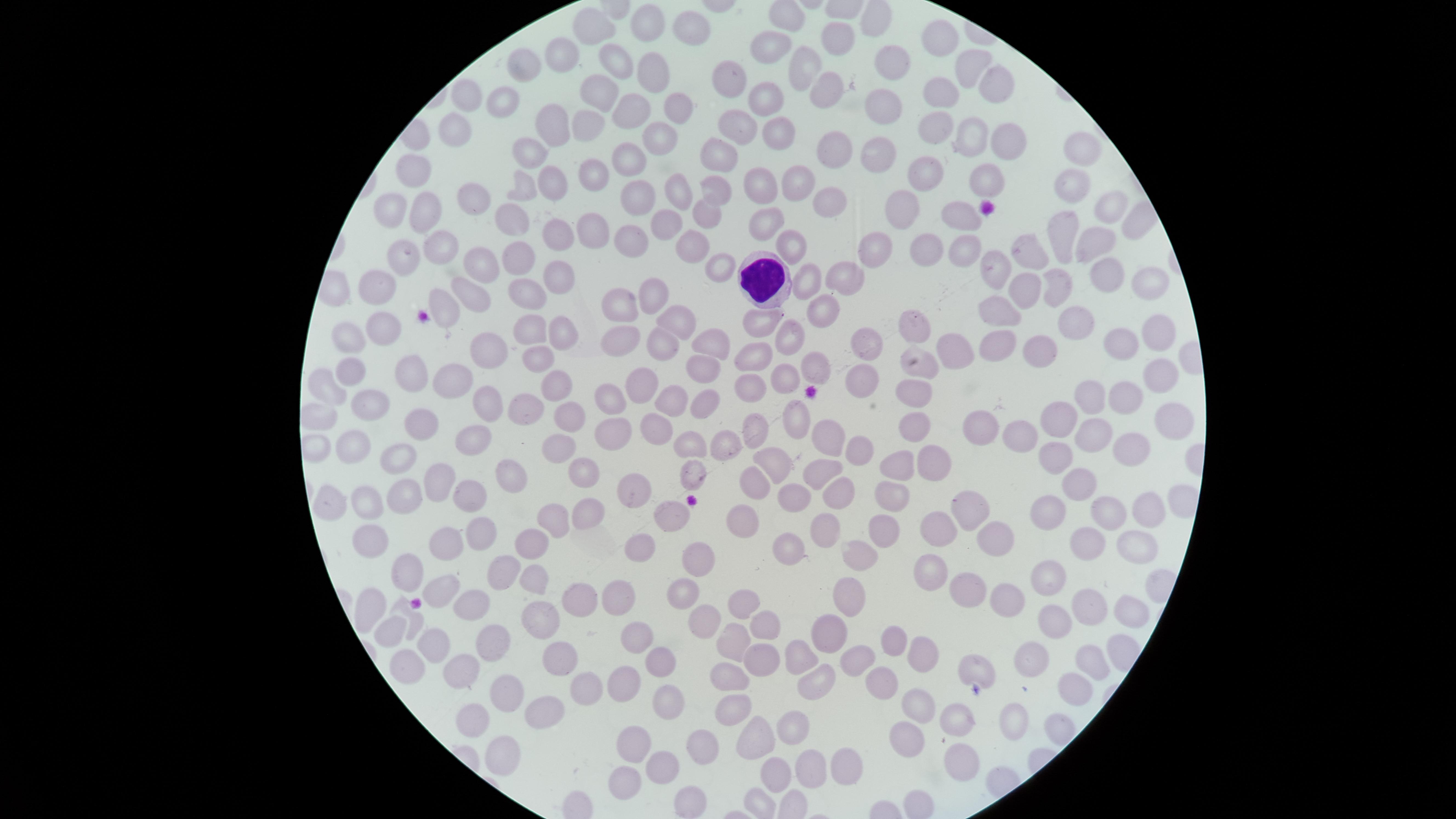
Approximate marker points as {x, y} in pixels. WBCs: {766, 276}. Uninfected RBCs: {782, 17}, {875, 23}, {649, 24}, {600, 27}, {690, 27}, {945, 37}, {839, 39}, {766, 46}, {530, 60}, {562, 61}, {889, 61}, {620, 62}, {808, 67}, {973, 68}, {655, 75}, {997, 81}, {726, 84}, {827, 87}, {943, 87}, {508, 93}, {469, 94}, {599, 95}, {885, 100}, {765, 102}, {672, 110}, {631, 114}, {455, 125}, {553, 125}, {735, 125}, {587, 126}, {774, 127}, {939, 131}, {998, 135}, {656, 136}, {968, 138}, {534, 148}, {717, 149}, {877, 149}, {829, 151}, {1079, 154}, {626, 163}, {419, 170}, {589, 173}, {552, 180}, {926, 180}, {983, 180}, {793, 182}, {764, 183}, {520, 184}, {1071, 188}, {679, 189}, {716, 189}, {473, 194}, {630, 194}, {830, 195}, {387, 202}, {1105, 207}, {960, 208}, {907, 209}, {417, 214}, {519, 214}, {708, 216}, {665, 222}, {769, 225}, {583, 231}, {553, 233}, {627, 234}, {1062, 238}, {1097, 242}, {791, 244}, {442, 246}, {696, 247}, {933, 249}, {395, 250}, {877, 250}, {518, 251}, {966, 251}, {1034, 254}, {992, 263}, {478, 264}, {719, 270}, {847, 272}, {1108, 273}, {561, 276}, {1149, 279}, {809, 280}, {380, 282}, {1028, 287}, {526, 288}, {1060, 288}, {653, 290}, {474, 298}, {623, 304}, {444, 308}, {827, 309}, {1001, 312}, {678, 318}, {379, 319}, {765, 320}, {1071, 325}, {920, 326}, {529, 327}, {561, 329}, {1150, 330}, {796, 335}, {621, 336}, {353, 342}, {704, 344}, {864, 344}, {660, 345}, {1114, 345}, {485, 347}, {1039, 348}, {956, 350}, {997, 351}, {756, 353}, {538, 355}, {923, 362}, {813, 365}, {351, 370}, {704, 372}, {405, 376}, {1156, 376}, {783, 378}, {557, 381}, {860, 381}, {448, 384}, {327, 386}, {644, 386}, {749, 387}, {918, 387}, {614, 394}, {1123, 395}, {1082, 398}, {670, 399}, {708, 401}, {488, 402}, {367, 403}, {530, 409}, {793, 415}, {322, 416}, {420, 417}, {569, 417}, {1053, 419}, {1177, 420}, {911, 421}, {980, 425}, {615, 429}, {751, 429}, {659, 433}, {821, 433}, {1091, 433}, {1016, 434}, {473, 438}, {722, 443}, {350, 444}, {692, 444}, {317, 445}, {555, 446}, {1132, 446}, {863, 454}, {1064, 454}, {389, 457}, {935, 457}, {781, 463}, {897, 464}, {827, 471}, {582, 472}, {509, 476}, {1085, 482}, {439, 483}, {758, 488}, {838, 490}, {891, 490}, {630, 492}, {470, 493}, {795, 494}, {394, 496}, {362, 503}, {1054, 503}, {330, 505}, {972, 505}, {1144, 510}, {673, 513}, {1118, 513}, {584, 515}, {551, 517}, {747, 521}, {827, 527}, {883, 528}, {940, 528}, {1089, 530}, {476, 532}, {439, 537}, {995, 537}, {368, 543}, {534, 546}, {636, 547}, {787, 549}, {1127, 553}, {856, 554}, {697, 555}, {503, 567}, {410, 573}, {932, 573}, {535, 575}, {1050, 577}, {443, 590}, {850, 592}, {966, 592}, {619, 595}, {680, 595}, {576, 596}, {746, 597}, {463, 601}, {371, 602}, {995, 602}, {1087, 604}, {1116, 606}, {713, 614}, {414, 619}, {1052, 621}, {540, 622}, {770, 624}, {828, 627}, {392, 630}, {733, 641}, {898, 641}, {493, 642}, {638, 642}, {432, 648}, {561, 651}, {755, 654}, {923, 655}, {798, 656}, {854, 660}, {1038, 660}, {1091, 660}, {403, 662}, {660, 662}, {971, 666}, {461, 670}, {732, 675}, {624, 680}, {815, 681}, {883, 681}, {1073, 684}, {509, 699}, {588, 699}, {662, 702}, {916, 706}, {734, 707}, {538, 714}, {1015, 715}, {476, 717}, {957, 718}, {1049, 723}, {791, 729}, {755, 737}, {909, 739}, {699, 744}, {635, 746}, {503, 758}, {846, 763}, {967, 763}, {662, 765}, {809, 766}, {778, 770}, {626, 784}, {681, 798}, {761, 807}. Giemsa-stained preparation. Image is 1456×819 pixels. Thin blood film. Circular visible region. Photographed with a smartphone camera through the microscope eyepiece. One field of view of the specimen. Presence: no malaria parasites detected.